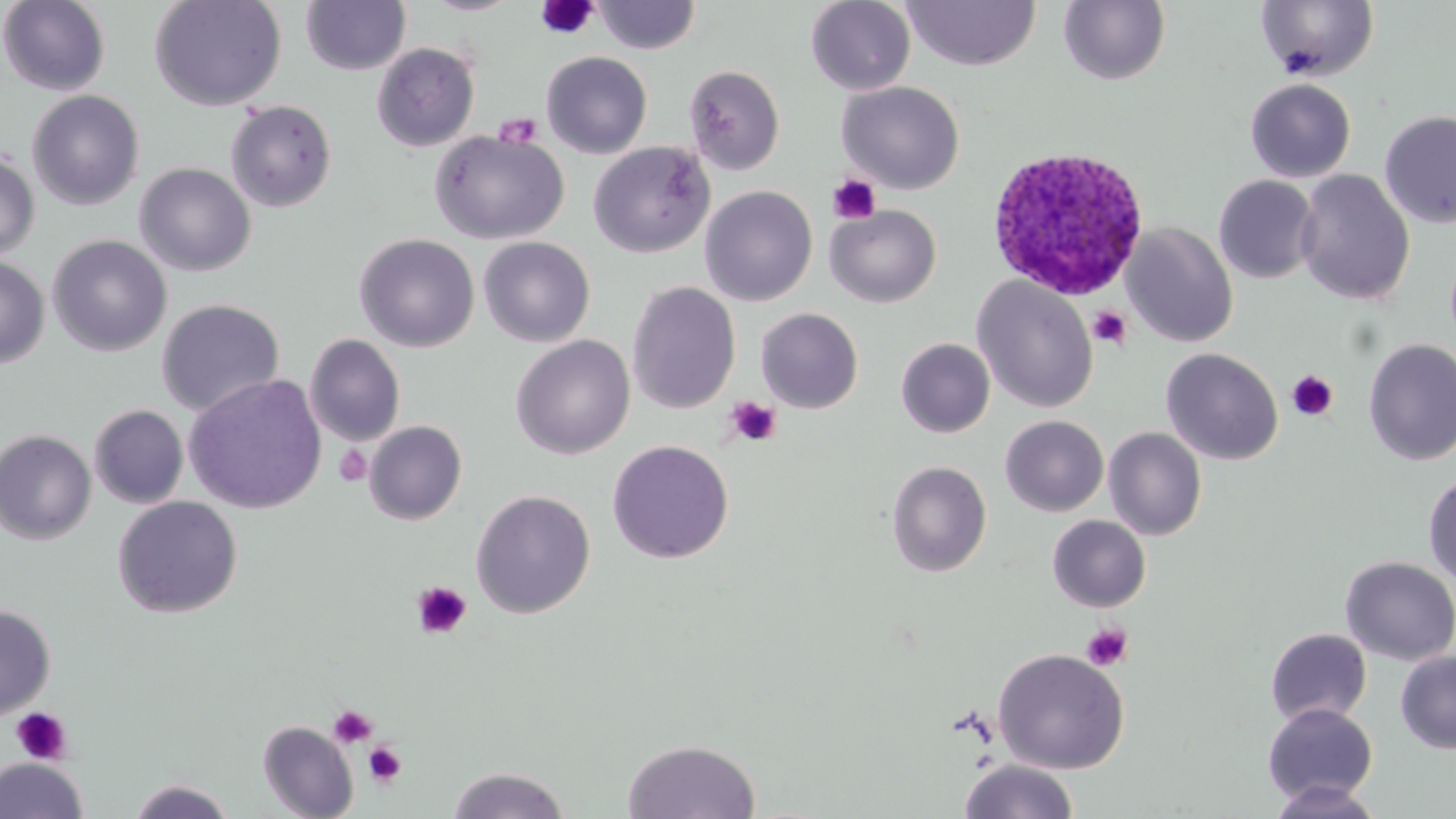
slide-level diagnosis = Plasmodium ovale
magnification = 1000x
platelet locations (subset) = approximate bounding boxes as [x1, y1, x2, y2] in pixels: [536, 1, 599, 40], [494, 113, 543, 149], [828, 174, 881, 224], [1087, 305, 1132, 350], [1286, 369, 1339, 421], [726, 396, 782, 446], [333, 444, 373, 487], [411, 580, 473, 640], [1082, 623, 1133, 671], [328, 705, 378, 748], [10, 708, 72, 764], [363, 742, 407, 788]
Plasmodium ovale-infected red blood cell locations = approximate bounding boxes as [x1, y1, x2, y2] in pixels: [986, 145, 1150, 301]
stain = May-Grünwald-Giemsa
field of view = single
preparation = thin blood film
uninfected red blood cell locations (subset) = approximate bounding boxes as [x1, y1, x2, y2] in pixels: [149, 0, 286, 112], [300, 0, 411, 75], [422, 0, 520, 15], [805, 0, 916, 95], [1, 1, 111, 96], [591, 1, 702, 54], [902, 1, 1041, 71], [1058, 1, 1171, 85], [1255, 1, 1379, 82], [371, 42, 480, 152], [541, 51, 653, 158], [686, 65, 786, 175], [1245, 79, 1356, 182], [837, 81, 965, 194], [26, 89, 145, 211], [225, 99, 338, 213], [1379, 110, 1456, 229], [428, 129, 569, 244], [588, 141, 715, 258], [0, 150, 40, 262], [134, 162, 256, 277], [1295, 170, 1415, 306], [1213, 175, 1321, 284], [699, 186, 818, 305], [825, 204, 941, 307], [1122, 222, 1238, 348], [354, 233, 480, 352], [47, 234, 172, 357], [478, 236, 595, 347], [0, 257, 49, 368], [972, 275, 1098, 413], [627, 281, 741, 414], [156, 298, 285, 416], [755, 307, 864, 413], [304, 334, 406, 447], [510, 335, 635, 460], [895, 338, 995, 438], [1362, 338, 1456, 466], [1161, 348, 1284, 465], [183, 373, 328, 514], [90, 405, 188, 509], [1000, 415, 1109, 516], [1104, 427, 1207, 540], [0, 429, 96, 545], [607, 440, 734, 564], [886, 460, 992, 577], [1423, 473, 1456, 588], [470, 489, 596, 618], [112, 496, 243, 619], [1047, 515, 1151, 612], [1339, 556, 1456, 665], [0, 604, 56, 720], [1265, 628, 1371, 727], [993, 648, 1129, 774], [1395, 650, 1456, 754], [1262, 703, 1378, 806], [258, 721, 358, 819], [622, 738, 761, 819], [0, 757, 88, 819], [959, 759, 1079, 819], [446, 766, 572, 818], [127, 778, 236, 819], [1266, 780, 1384, 818]
image size = 1456×819 pixels
modality = light microscopy